Locate every blood parasite and identify its species.
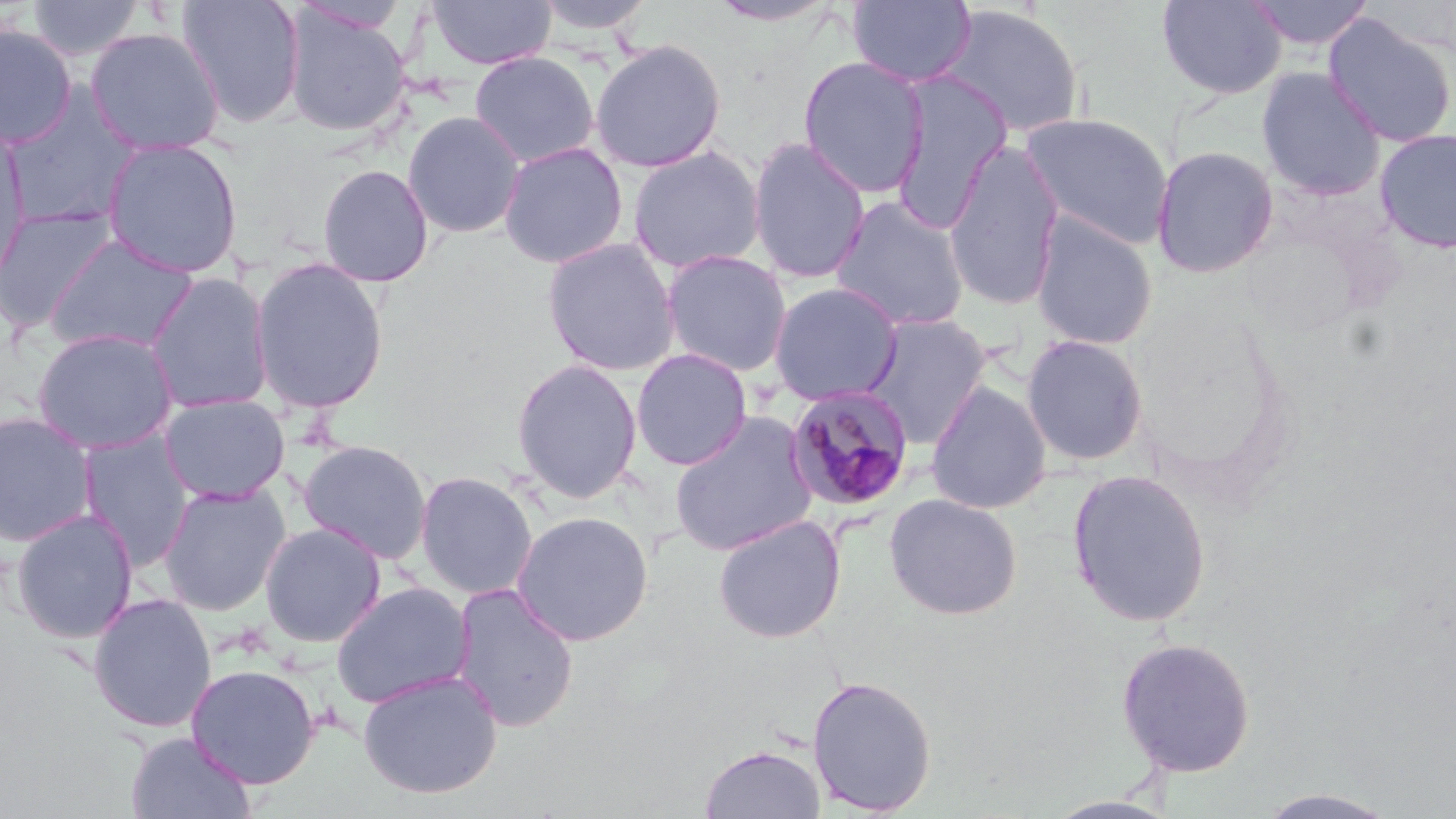

Approximate bounding boxes as (x1,y1)-(x2,y2) corner pairs in pixels.
Plasmodium malariae-infected red blood cells: (784,385)-(916,513).
No Plasmodium falciparum, Plasmodium ovale, Plasmodium vivax, Babesia divergens, or Trypanosoma brucei observed.

slide_level_diagnosis: Plasmodium malariae
modality: light microscopy
image_size: 1456×819 pixels
uninfected_red_blood_cell_locations: 'approximate bounding boxes as (x1,y1)-(x2,y2) corner pairs in pixels: (26,0)-(145,61), (175,0)-(306,129), (427,0)-(556,70), (531,0)-(657,35), (848,0)-(977,88), (1155,0)-(1288,101), (1244,0)-(1375,51), (707,1)-(841,28), (934,3)-(1086,139), (282,5)-(412,138), (1322,14)-(1456,148), (0,22)-(77,148), (86,27)-(225,156), (589,38)-(727,173), (469,51)-(600,168), (797,55)-(930,198), (1256,67)-(1386,201), (889,70)-(1013,232), (2,85)-(143,228), (402,110)-(525,239), (1019,112)-(1174,249), (0,123)-(32,286), (1374,128)-(1456,253), (101,137)-(243,278), (747,137)-(871,285), (942,140)-(1067,311), (498,141)-(629,269), (627,145)-(766,274), (1150,145)-(1280,279), (317,163)-(434,287), (829,195)-(972,333), (0,205)-(119,332), (1029,212)-(1159,352), (43,234)-(200,355), (542,237)-(682,377), (659,249)-(793,378), (250,257)-(389,414), (145,272)-(275,414), (768,281)-(905,406), (859,312)-(993,449), (31,327)-(180,455), (1020,333)-(1150,467), (631,348)-(754,471), (510,357)-(644,503), (925,380)-(1052,515), (159,394)-(291,504), (0,411)-(100,547), (669,411)-(819,556), (77,431)-(196,570), (298,439)-(432,564), (1066,468)-(1213,628), (414,470)-(539,600), (158,482)-(291,616), (883,492)-(1023,620), (10,508)-(139,644), (511,510)-(654,646), (712,514)-(846,643), (259,522)-(386,647), (331,581)-(475,709), (449,582)-(581,733), (87,592)-(217,733), (1115,636)-(1256,777), (185,663)-(321,789), (357,669)-(503,800), (806,675)-(938,816), (125,731)-(256,818), (699,743)-(826,819), (1252,788)-(1402,818)'
field_of_view: single
magnification: 1000x
preparation: thin blood film
stain: May-Grünwald-Giemsa